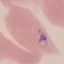

Summary:
  - Malaria status: parasitized
  - Stain: Giemsa
  - Capture: smartphone through the microscope eyepiece
  - Preparation: thin blood smear
  - Image type: automatically extracted cell patch, resized to 64 × 64 pixels